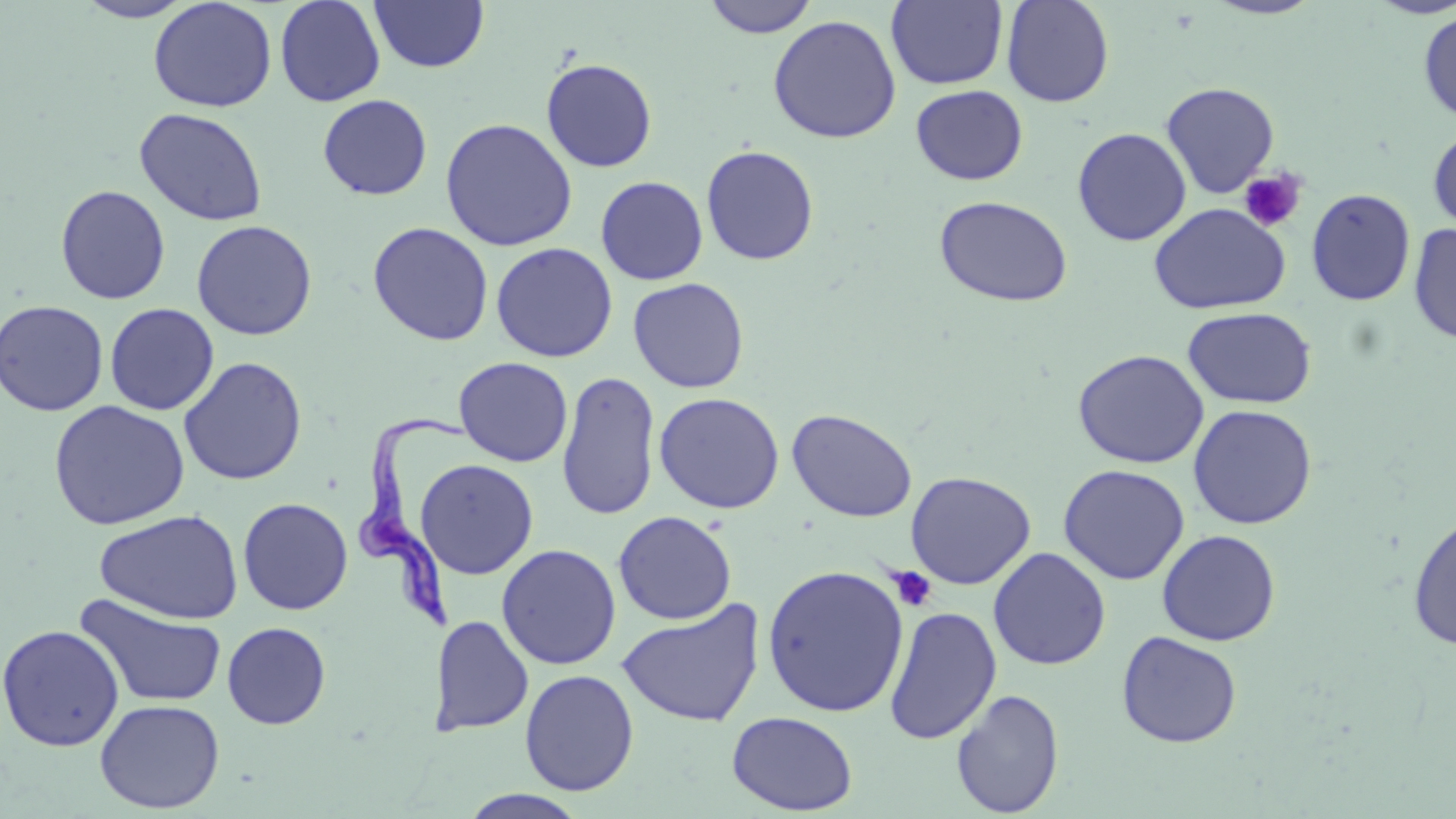 Approximate bounding boxes as [x1, y1, x2, y2] in pixels. Uninfected red blood cell locations (subset): [74, 0, 195, 23], [148, 0, 278, 113], [275, 0, 386, 107], [369, 0, 489, 73], [701, 0, 820, 38], [886, 0, 1008, 90], [1001, 0, 1115, 108], [1202, 0, 1326, 20], [1417, 11, 1456, 125], [767, 14, 902, 143], [541, 57, 658, 172], [910, 84, 1028, 185], [317, 94, 433, 200], [134, 107, 268, 227], [439, 117, 578, 251], [1428, 125, 1456, 234], [1072, 127, 1192, 246], [701, 145, 819, 266], [595, 176, 709, 285], [55, 184, 171, 304], [1306, 188, 1416, 306], [933, 195, 1072, 307], [1148, 203, 1290, 315], [191, 219, 318, 341], [367, 221, 494, 346], [1408, 224, 1456, 344], [490, 242, 618, 362], [628, 277, 749, 393], [0, 299, 109, 416], [104, 303, 219, 415], [1182, 307, 1317, 409], [1073, 349, 1210, 469], [178, 356, 307, 486], [454, 357, 573, 467], [556, 370, 662, 521], [654, 392, 785, 514], [48, 400, 190, 530], [1187, 404, 1317, 529], [787, 408, 918, 522], [414, 458, 539, 580], [1058, 464, 1190, 585], [905, 471, 1036, 589], [238, 497, 353, 615], [94, 509, 244, 624], [613, 510, 737, 625], [1407, 513, 1456, 651], [1157, 529, 1281, 646], [497, 544, 621, 670], [989, 547, 1111, 670], [762, 564, 910, 718], [75, 593, 228, 709], [617, 599, 764, 728], [884, 606, 1002, 745], [432, 615, 534, 737], [222, 622, 331, 729], [0, 624, 125, 751], [1116, 630, 1243, 748], [519, 669, 639, 795], [951, 688, 1064, 817], [95, 698, 225, 814], [726, 710, 858, 815], [456, 789, 591, 819]. Platelet locations (subset): [1238, 168, 1306, 233], [887, 566, 937, 612]. Trypanosoma brucei locations: [348, 402, 473, 633]. Slide-level diagnosis: Trypanosoma brucei. One field of a larger specimen. May-Grünwald-Giemsa-stained preparation. Light microscopy. Captured at 1000x magnification. Image is 1456×819 pixels. Thin blood smear.